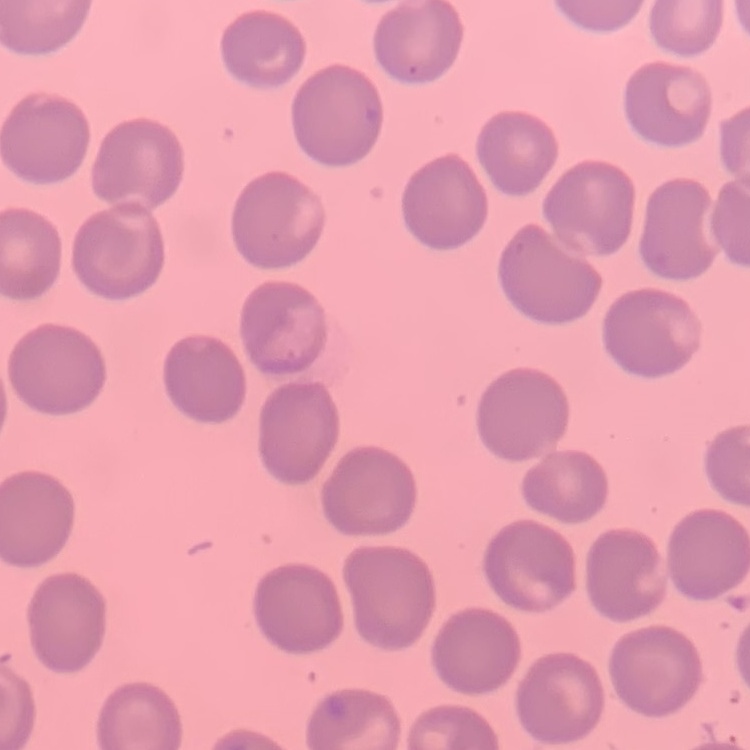

Summary:
  - Red blood cell morphology: no rouleaux formation
  - Image type: one tile cut from a larger photomicrograph
  - Stain: Field's or Giemsa
  - Preparation: thin blood film